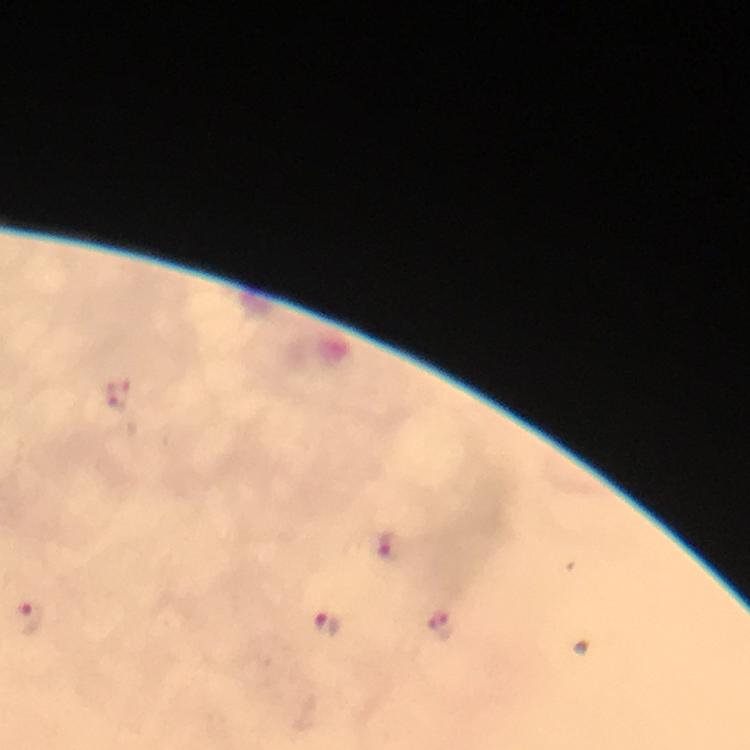
Approximate centers as [x, y] in pixels.
Summary:
  - Plasmodium parasite locations: [117, 395], [387, 544], [28, 619], [325, 623], [441, 624]
  - Preparation: thick blood smear
  - Magnification: 100x
  - Image size: 750×750 pixels
  - Context: from a diagnostic examination for malaria
  - Immersion oil: applied
  - Stain: Giemsa
  - Capture: smartphone camera through the microscope
  - Cropped from: one field of view